Give the position of each Plasmodium falciparum parasite with its life-cycle stage, each leukocyte, and any debris.
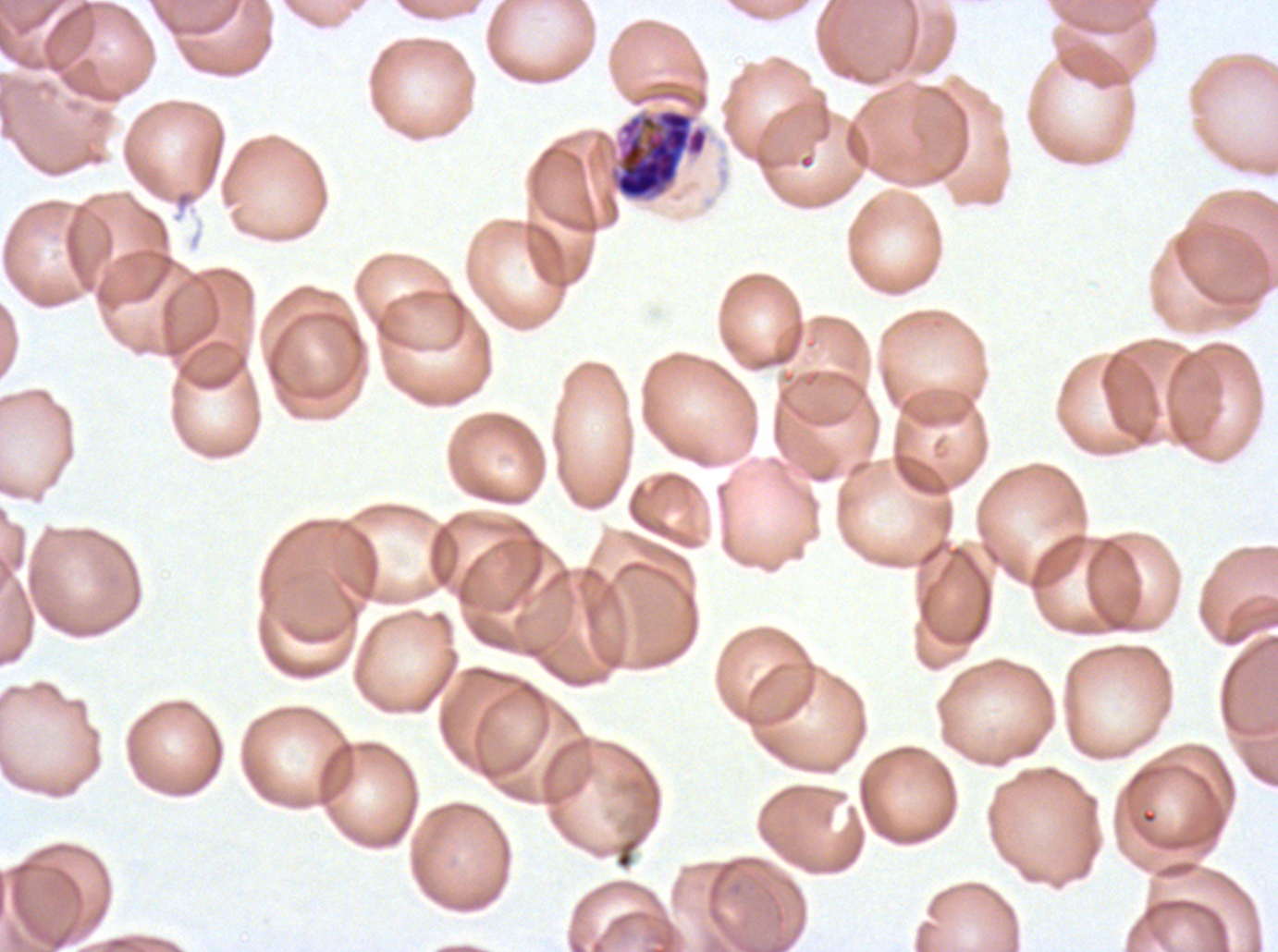
Approximate bounding boxes as (x1, y1, x2, y2) in pixels.
Late schizonts: (613, 108, 708, 201).
No rings, late-ring/early-trophozoite forms, mid trophozoites, late trophozoites, early schizonts, segmenters, gametocytes, leukocytes, or debris observed.

image size = 1278×952 pixels
preparation = thin blood film
specimen = ex-vivo Plasmodium falciparum culture from a patient in The Gambia, grown for 24 to 48 hours
stain = Giemsa
field of view = sub-image separated from a larger composite